Identify the parasite.
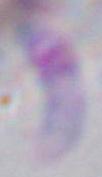
Toxoplasma gondii.

{
  "modality": "micrograph",
  "magnification": "1000x"
}